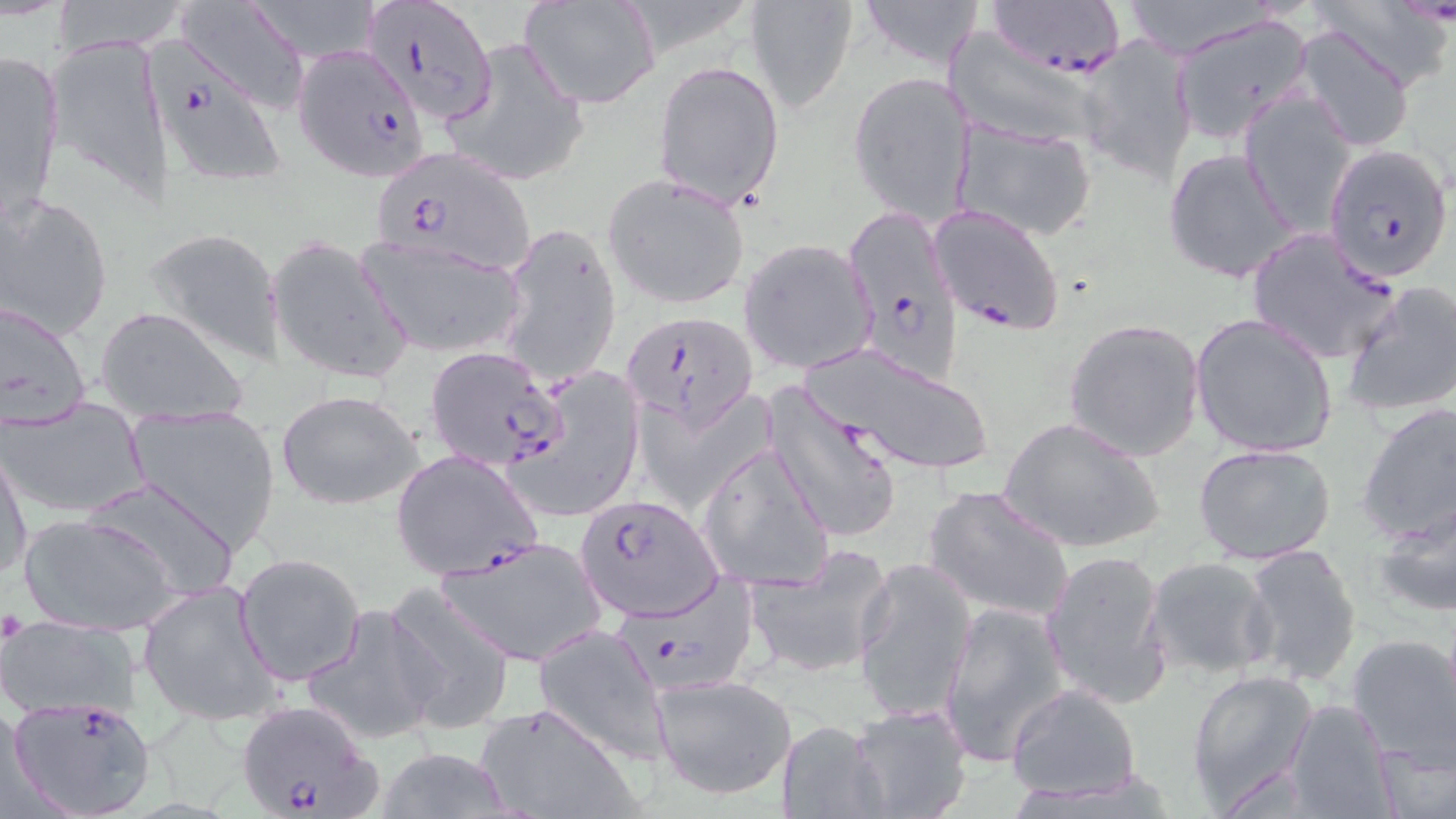
Approximate bounding boxes as (x1, y1, x2, y2) in pixels. Uninfected red blood cell locations: (46, 0, 197, 53), (174, 0, 310, 114), (520, 0, 662, 109), (744, 0, 860, 115), (856, 0, 985, 70), (1112, 0, 1271, 58), (1300, 0, 1453, 93), (1169, 13, 1313, 145), (1291, 26, 1417, 152), (940, 31, 1115, 152), (42, 33, 175, 206), (1074, 33, 1201, 185), (440, 36, 589, 189), (1, 49, 66, 217), (653, 60, 785, 209), (846, 69, 976, 226), (1237, 91, 1356, 235), (950, 118, 1098, 242), (1163, 147, 1300, 285), (602, 173, 752, 310), (2, 191, 114, 341), (499, 220, 622, 385), (142, 228, 286, 365), (267, 235, 412, 386), (357, 235, 528, 359), (739, 238, 877, 375), (1341, 280, 1456, 419), (0, 296, 94, 432), (95, 305, 248, 424), (1189, 312, 1338, 459), (1061, 317, 1208, 461), (804, 340, 997, 479), (511, 363, 644, 522), (765, 387, 905, 546), (276, 389, 426, 509), (3, 398, 150, 519), (1355, 401, 1456, 549), (125, 404, 283, 555), (999, 416, 1164, 558), (695, 441, 835, 593), (1193, 443, 1337, 568), (0, 446, 31, 586), (81, 477, 240, 603), (922, 484, 1075, 623), (1371, 499, 1456, 620), (19, 512, 179, 634), (437, 533, 609, 665), (1239, 544, 1365, 688), (744, 547, 894, 680), (1042, 547, 1173, 710), (233, 552, 366, 686), (852, 555, 978, 724), (1143, 555, 1279, 680), (137, 581, 283, 726), (382, 583, 516, 734), (938, 601, 1069, 767), (302, 602, 444, 746), (0, 622, 142, 720), (534, 623, 672, 765), (1348, 633, 1456, 767), (1187, 669, 1318, 808), (652, 670, 796, 799), (1005, 684, 1142, 804), (1283, 700, 1398, 818), (476, 701, 638, 819), (845, 701, 975, 819), (774, 716, 888, 817), (1375, 740, 1456, 819), (377, 746, 519, 819). Plasmodium falciparum-infected red blood cell locations: (986, 0, 1127, 76), (359, 3, 491, 129), (292, 41, 428, 180), (149, 55, 291, 188), (1322, 145, 1453, 283), (369, 148, 534, 273), (928, 204, 1065, 335), (850, 213, 968, 390), (1246, 227, 1401, 365), (622, 309, 755, 429), (426, 346, 568, 474), (392, 449, 542, 582), (573, 494, 721, 622), (605, 570, 755, 697), (3, 695, 159, 818), (235, 699, 384, 819). Slide-level diagnosis: Plasmodium falciparum. Captured at 1000x magnification. Thin blood smear. One field of a larger specimen. Image is 1456×819 pixels. Light microscopy. May-Grünwald-Giemsa-stained preparation.